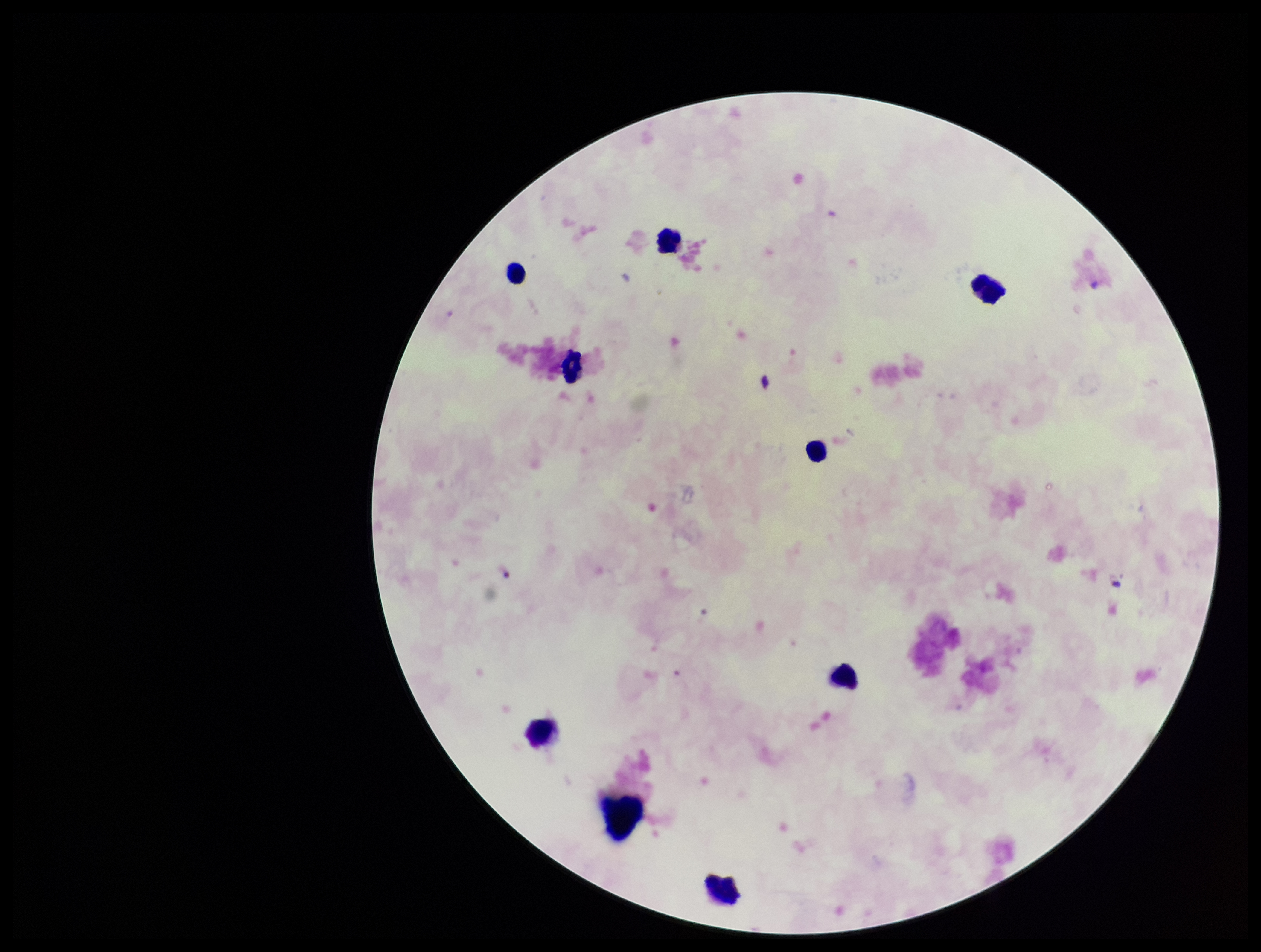

Summary:
  - Image size: 1261×952 pixels
  - Plasmodium parasites: none detected
  - Preparation: thick blood smear
  - Field of view: one from this slide
  - Stain: Giemsa
  - Parasite count: 0
  - Capture: smartphone photograph through the microscope eyepiece
  - Leukocyte count: 8
  - Patient malaria status: negative